State which parasite is depicted.
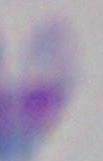

This is Toxoplasma gondii.

1000x magnification. Micrograph.